Name the parasite shown.
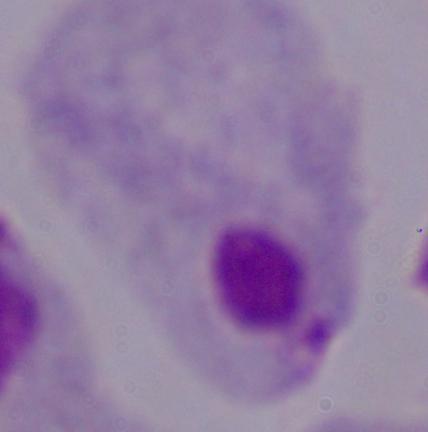
A trichomonad.

modality = photomicrograph
magnification = 1000x